Assess this cell for malaria.
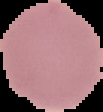

Uninfected.

Segmented cell region on a black background. From a thin blood smear. Image is 103×112 pixels.